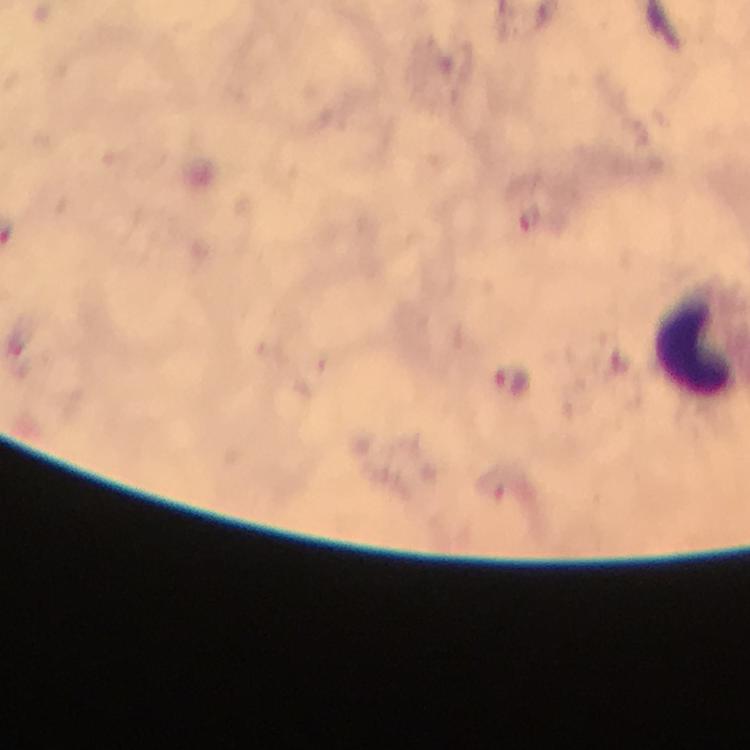
Approximate centers as (x, y) in pixels.
Summary:
  - Plasmodium parasite locations: (512, 380)
  - Immersion oil: used
  - Stain: Giemsa
  - Context: from a malaria diagnostic workup
  - Cropped from: one field of view
  - Image size: 750×750 pixels
  - Magnification: 100x
  - Preparation: thick blood film
  - Capture: smartphone mounted on the microscope